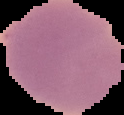

From a thin blood film. Image is 124×115 pixels. Malaria status: uninfected. The area outside the segmented cell region is set to black.